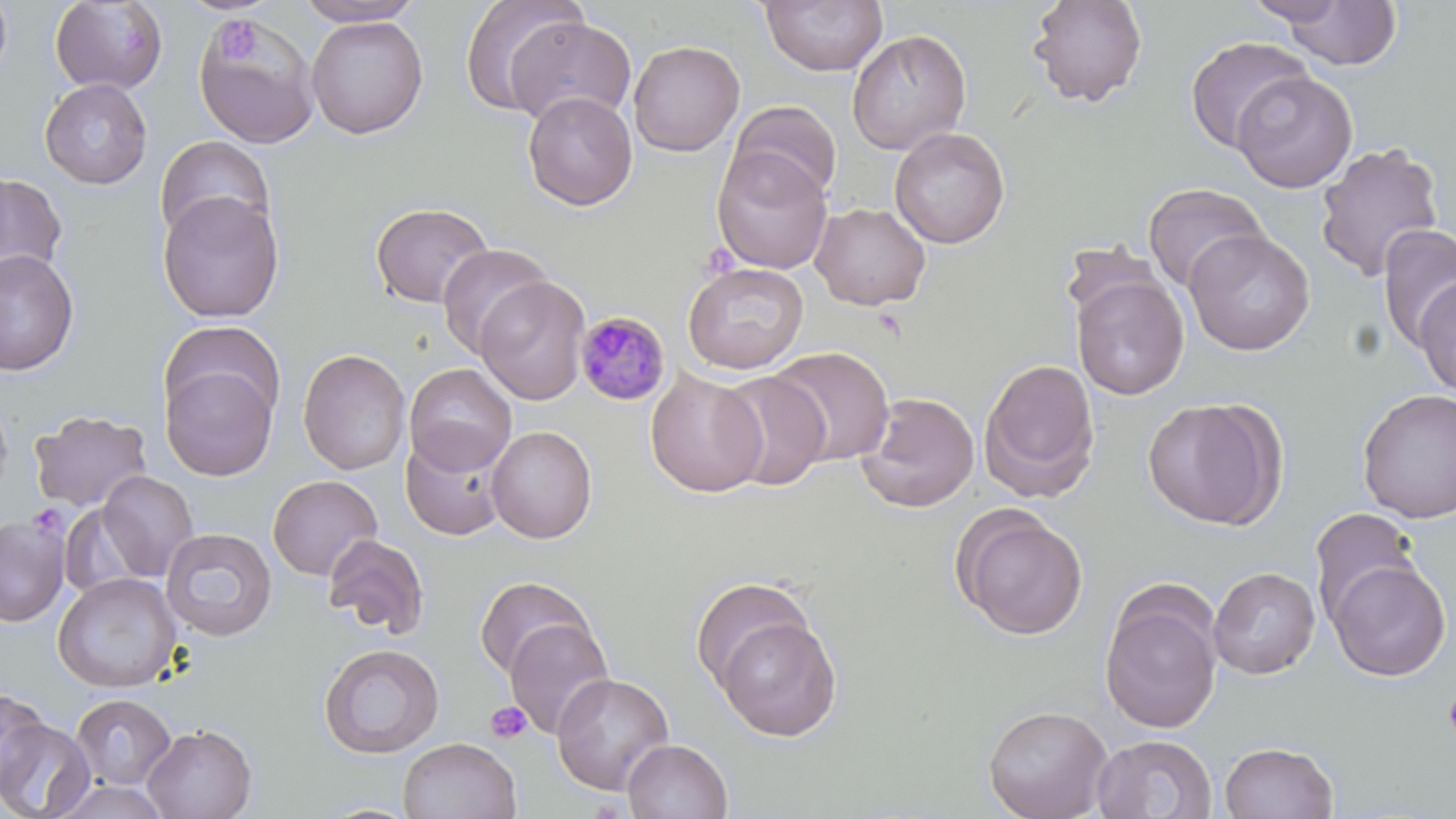 Approximate bounding boxes as [x1, y1, x2, y2] in pixels. Plasmodium malariae-infected red blood cell locations: [574, 311, 670, 407]. Platelet locations: [216, 21, 258, 64], [1442, 690, 1456, 741], [486, 701, 532, 744]. Uninfected red blood cell locations: [0, 0, 13, 87], [293, 0, 427, 26], [458, 0, 587, 118], [1026, 0, 1148, 108], [1244, 0, 1351, 25], [50, 1, 169, 94], [758, 1, 888, 77], [1279, 1, 1403, 69], [193, 12, 321, 149], [305, 14, 429, 139], [504, 15, 637, 127], [846, 29, 972, 156], [1184, 35, 1312, 154], [628, 40, 745, 157], [1231, 70, 1357, 194], [39, 77, 153, 189], [522, 91, 638, 211], [728, 100, 842, 204], [889, 126, 1010, 249], [155, 134, 275, 245], [1314, 141, 1445, 283], [711, 147, 833, 274], [0, 172, 67, 285], [1142, 183, 1268, 293], [157, 191, 284, 324], [370, 202, 494, 310], [810, 202, 931, 311], [1377, 223, 1456, 353], [1183, 229, 1316, 356], [437, 243, 553, 357], [0, 249, 79, 377], [682, 262, 809, 375], [1071, 273, 1189, 401], [475, 275, 591, 405], [1413, 277, 1456, 398], [160, 319, 285, 430], [769, 346, 896, 466], [298, 348, 410, 475], [978, 358, 1101, 501], [160, 361, 278, 482], [404, 363, 517, 475], [645, 368, 767, 498], [716, 370, 831, 491], [1356, 388, 1456, 524], [855, 391, 980, 514], [0, 392, 14, 502], [1143, 397, 1285, 530], [28, 409, 152, 513], [486, 425, 598, 543], [400, 431, 508, 542], [96, 471, 199, 581], [267, 474, 383, 581], [953, 507, 1088, 641], [1308, 507, 1422, 628], [1, 513, 70, 626], [160, 527, 278, 642], [322, 533, 430, 639], [1326, 559, 1451, 681], [1208, 566, 1320, 679], [53, 572, 181, 693], [474, 575, 595, 681], [690, 575, 817, 692], [1098, 584, 1224, 735], [713, 615, 842, 741], [503, 617, 614, 739], [318, 643, 445, 759], [551, 673, 674, 796], [0, 687, 49, 794], [70, 693, 176, 790], [982, 703, 1113, 819], [0, 719, 95, 819], [142, 723, 257, 819], [1092, 734, 1217, 818], [398, 736, 522, 819], [622, 738, 733, 819], [1219, 740, 1339, 819], [49, 779, 172, 819]. Slide-level diagnosis: Plasmodium malariae. Single field of view. Image is 1456×819 pixels. May-Grünwald-Giemsa stain. Light microscopy. Captured at 1000x magnification. Thin blood smear.